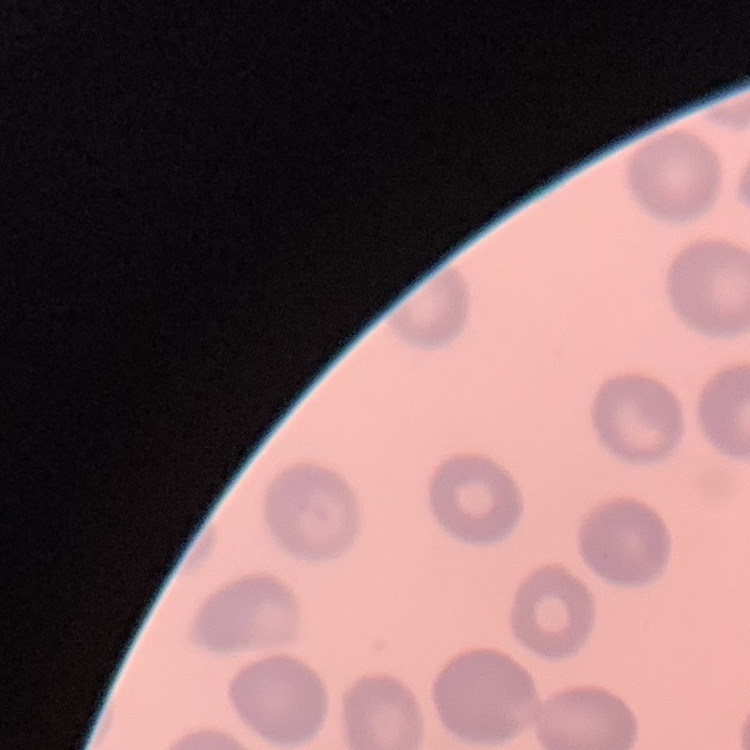
The erythrocytes exhibit no rouleaux formation. Field's or Giemsa stain. Thin peripheral smear. Square crop of a larger photomicrograph.